Assess the morphology of the red blood cells.
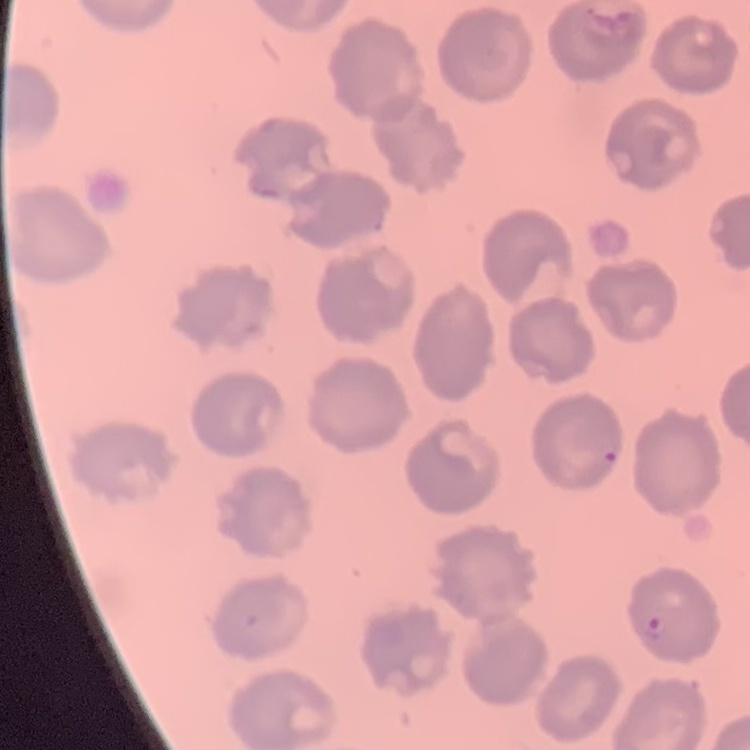

No rouleaux formation.

Summary:
  - Stain: Field's or Giemsa
  - Image type: square crop of a larger photomicrograph
  - Preparation: thin blood film